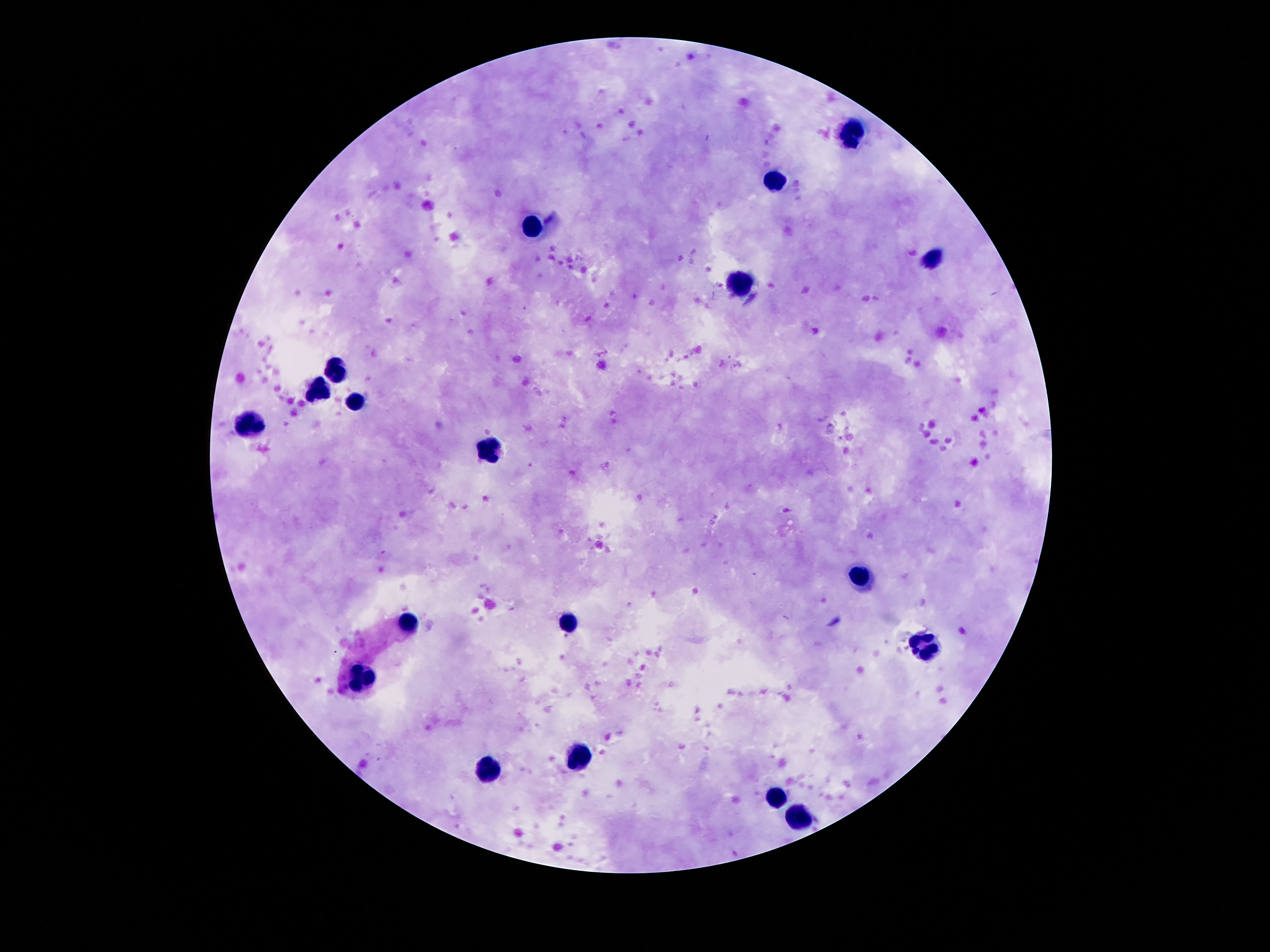

Approximate centers as {x, y} in pixels.
Summary:
  - Leukocyte locations: {849, 131}, {771, 183}, {531, 227}, {932, 258}, {741, 283}, {335, 369}, {319, 390}, {358, 402}, {251, 426}, {489, 448}, {860, 579}, {569, 623}, {407, 624}, {925, 645}, {365, 679}, {580, 754}, {485, 773}, {774, 797}, {800, 815}
  - Magnification: 100x
  - Preparation: thick blood smear
  - Image size: 1270×952 pixels
  - Capture: smartphone camera through the microscope eyepiece
  - Patient malaria status: negative
  - Field of view: single
  - Stain: Giemsa